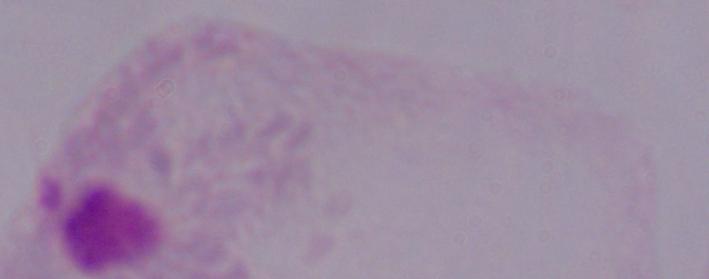 1000x magnification. Micrograph. A trichomonad is shown.